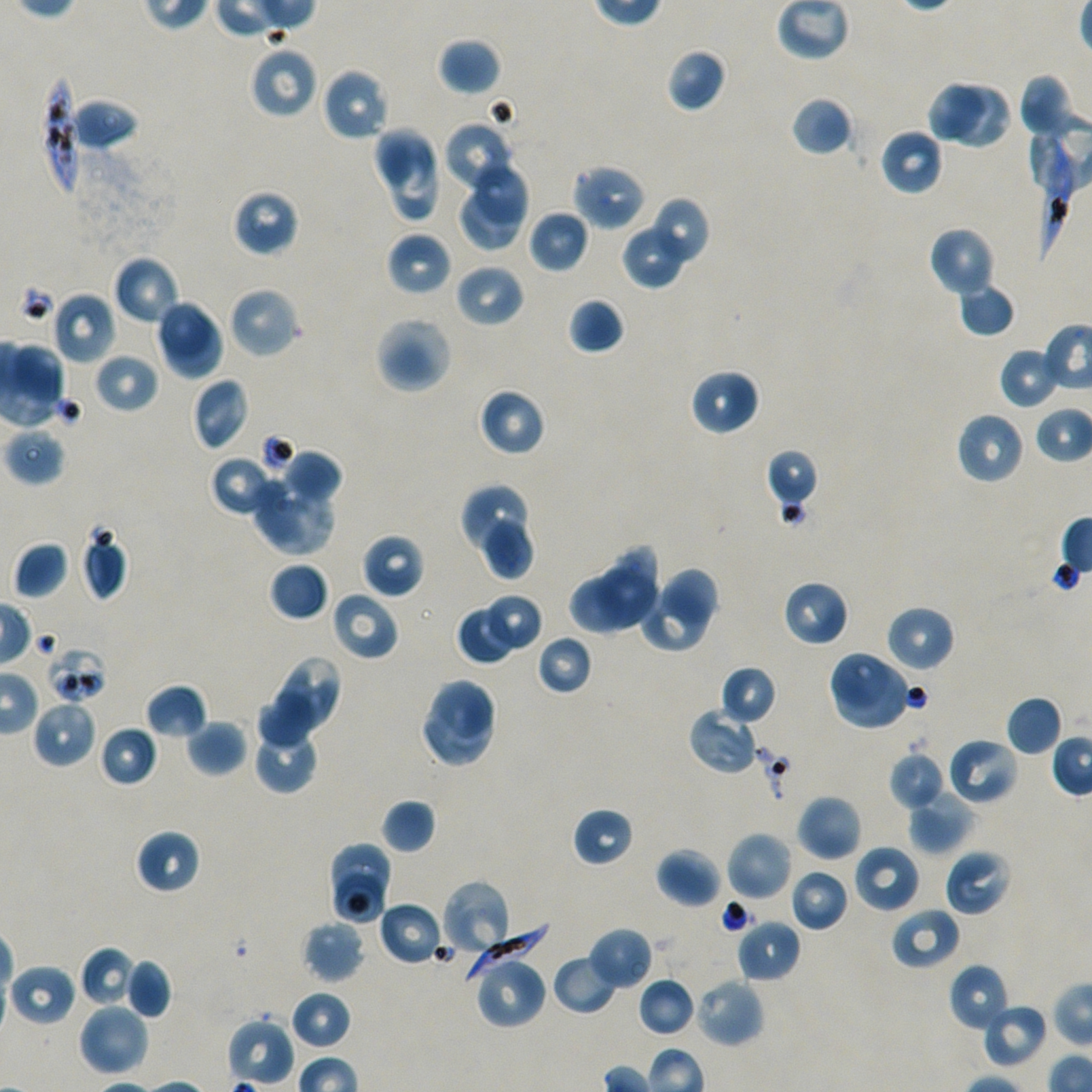
Not every red blood cell is marked.
{
  "stain": "Giemsa",
  "objective": "100x, oil immersion, numerical aperture 1.45",
  "field_of_view": "one from this slide",
  "image_size": "1092×1092 pixels",
  "preparation": "thin blood smear",
  "donor_blood_group": "A+/O+",
  "locations_of_red_blood_cells_of_indeterminate_infection_status": "approximate bounding boxes as (x1, y1, x2, y2) in pixels: (45, 646, 108, 704)",
  "locations_of_infected_red_blood_cells": "approximate bounding boxes as (x1, y1, x2, y2) in pixels: (40, 73, 81, 199), (1033, 124, 1073, 261), (463, 918, 550, 978)",
  "culture": "static in-vitro P. falciparum strain NF54",
  "locations_of_uninfected_red_blood_cells": "approximate bounding boxes as (x1, y1, x2, y2) in pixels: (437, 37, 502, 96), (249, 43, 318, 120), (666, 48, 727, 113), (321, 67, 390, 142), (1017, 73, 1076, 139), (926, 81, 985, 141), (954, 83, 1009, 147), (790, 96, 854, 156), (69, 98, 139, 152), (443, 120, 517, 194), (372, 126, 435, 188), (879, 128, 944, 196), (381, 136, 443, 221), (472, 162, 530, 227), (572, 164, 647, 231), (460, 185, 520, 251), (232, 189, 299, 257), (646, 196, 710, 269), (528, 209, 589, 274), (928, 225, 996, 297), (621, 230, 684, 290), (386, 231, 452, 297), (112, 255, 181, 326), (454, 263, 525, 329), (957, 282, 1016, 337), (227, 285, 301, 360), (51, 291, 116, 365), (567, 296, 625, 355), (155, 298, 212, 359), (165, 315, 223, 378), (374, 315, 454, 394), (11, 342, 67, 405), (998, 345, 1061, 410), (93, 352, 159, 414), (689, 368, 761, 437), (190, 378, 249, 452), (478, 387, 547, 456), (956, 411, 1026, 485), (4, 428, 65, 486), (765, 448, 820, 511), (280, 449, 342, 507), (210, 454, 278, 517), (250, 476, 335, 555), (459, 485, 528, 550), (481, 518, 535, 582), (80, 530, 128, 601), (361, 533, 424, 599), (12, 542, 69, 599), (608, 546, 657, 597), (269, 562, 329, 622), (594, 564, 657, 629), (661, 568, 719, 629), (568, 575, 625, 635), (782, 580, 849, 647), (638, 587, 708, 654), (330, 590, 399, 661), (481, 593, 539, 648), (884, 604, 956, 672), (458, 611, 514, 664), (535, 634, 594, 695), (826, 649, 892, 711), (276, 655, 343, 729), (833, 663, 912, 731), (720, 665, 778, 725), (429, 678, 498, 744), (145, 683, 208, 740), (257, 692, 318, 747), (1005, 695, 1063, 756), (32, 699, 98, 769), (423, 702, 494, 769), (687, 707, 759, 776), (186, 719, 248, 776), (98, 725, 158, 786), (257, 729, 318, 795), (947, 737, 1019, 805), (888, 750, 946, 811), (907, 790, 973, 855), (796, 794, 862, 861), (380, 798, 436, 854), (571, 807, 635, 868), (134, 829, 201, 894), (726, 831, 793, 902), (330, 841, 394, 900), (853, 844, 921, 913), (656, 847, 723, 908), (943, 849, 1011, 916), (788, 868, 850, 932), (334, 872, 385, 924), (440, 879, 513, 957), (378, 900, 444, 966), (890, 907, 961, 970), (735, 917, 801, 983), (301, 920, 365, 984), (587, 927, 654, 990), (79, 945, 137, 1008), (551, 953, 619, 1015), (473, 956, 547, 1030), (124, 958, 172, 1019), (8, 963, 77, 1027), (948, 963, 1011, 1034), (637, 977, 696, 1037), (693, 977, 765, 1048), (290, 991, 352, 1049), (77, 1002, 149, 1077), (981, 1003, 1048, 1069), (227, 1017, 295, 1087)"
}